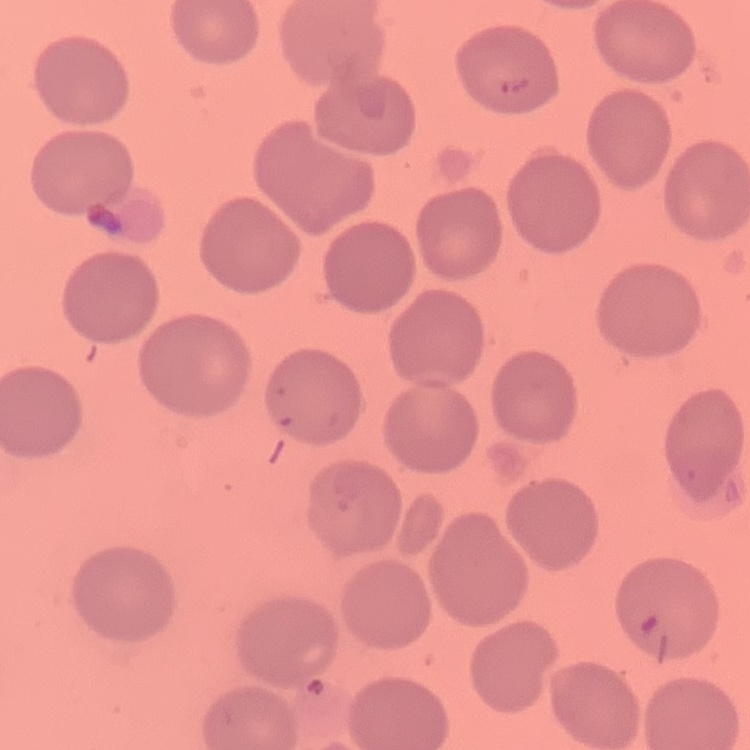

The red blood cells show no rouleaux formation. Stained with either Field's or Giemsa. One tile cut from a larger photomicrograph. Thin blood smear.